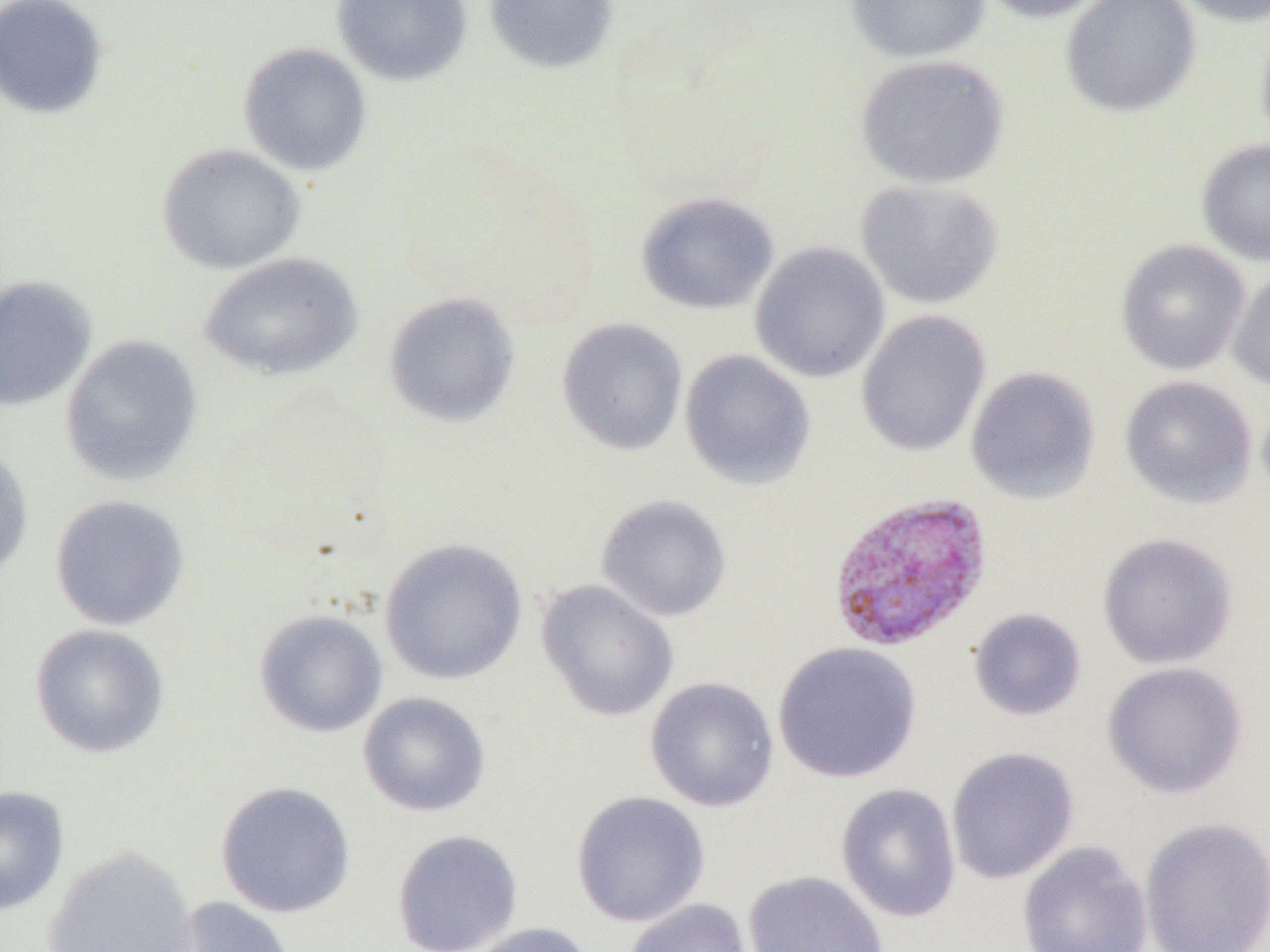

Approximate bounding boxes as (x1,y1)-(x2,y2) corner pairs in pixels. Uninfected red blood cell locations: (0,0)-(109,120), (332,0)-(472,85), (483,0)-(619,74), (846,0)-(991,63), (977,0)-(1114,23), (1061,0)-(1202,119), (1170,0)-(1270,27), (1255,18)-(1270,153), (237,42)-(372,175), (854,54)-(1010,190), (1196,138)-(1270,266), (157,143)-(305,274), (855,179)-(1004,310), (636,192)-(779,315), (1115,239)-(1251,375), (749,241)-(890,383), (199,252)-(363,382), (1228,266)-(1270,392), (0,276)-(96,412), (383,292)-(521,428), (855,310)-(991,457), (557,318)-(689,456), (59,335)-(203,486), (679,349)-(816,490), (965,366)-(1101,505), (1120,375)-(1258,509), (0,443)-(34,583), (49,494)-(190,631), (595,495)-(733,622), (1097,532)-(1238,669), (379,538)-(528,686), (535,580)-(679,722), (969,608)-(1087,721), (254,610)-(388,737), (29,624)-(169,758), (772,641)-(922,784), (1103,661)-(1248,798), (645,677)-(779,812), (358,692)-(490,817), (946,747)-(1080,884), (215,781)-(356,918), (836,783)-(962,923), (0,786)-(69,916), (571,791)-(710,928), (1138,816)-(1270,952), (392,830)-(524,952), (1017,841)-(1153,952), (41,846)-(198,952), (601,853)-(735,943), (743,870)-(889,952), (167,897)-(297,952), (623,898)-(754,952), (466,922)-(599,952). Plasmodium vivax-infected red blood cell locations: (827,492)-(994,652). Slide-level diagnosis: Plasmodium vivax. Thin blood smear. Image is 1270×952 pixels. Light microscopy. Single field of view. 1000x magnification.